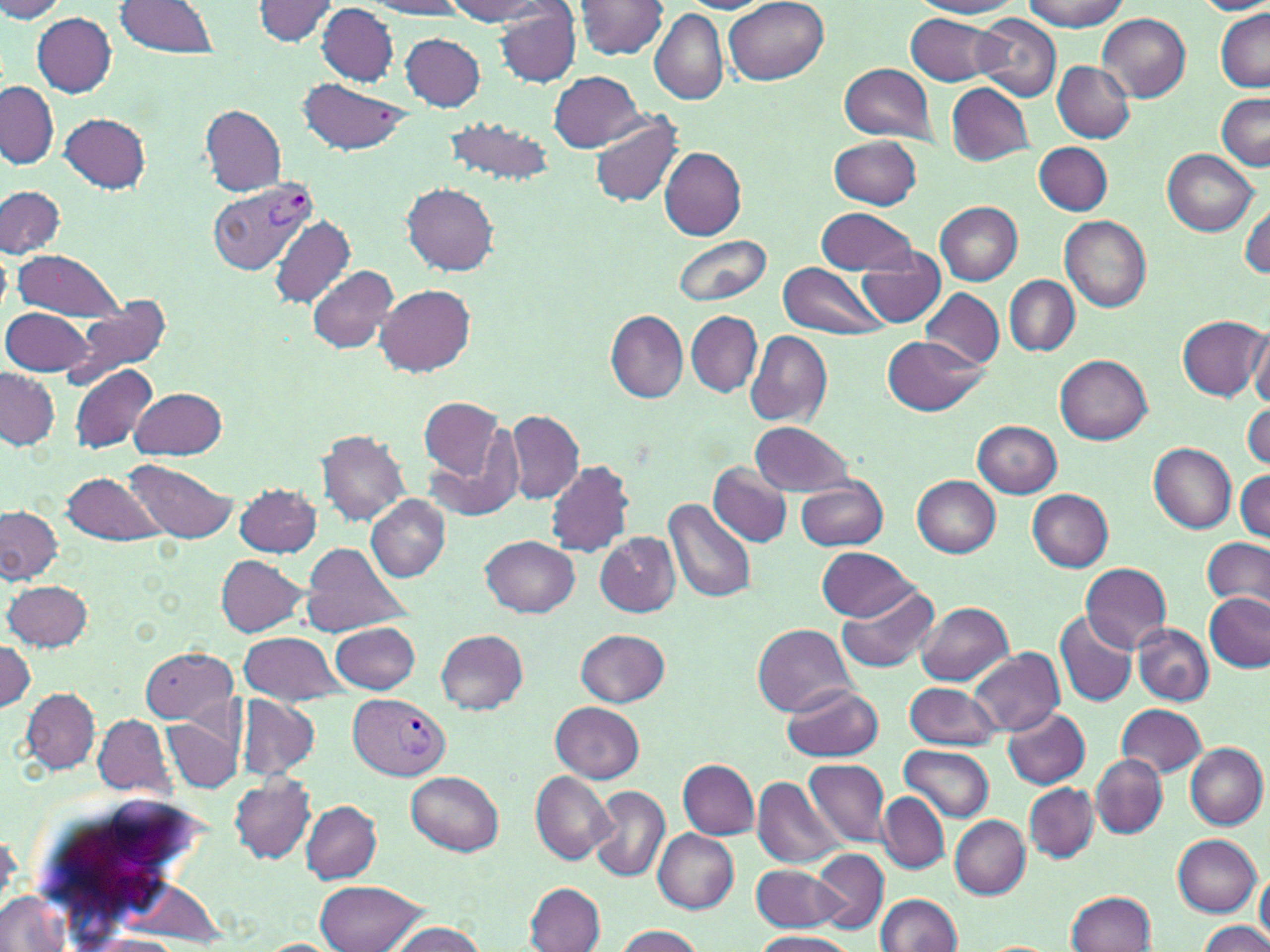

Summary:
  - Coordinate format: approximate bounding boxes as named x1/y1/x2/y2 corners in pixels
  - Plasmodium vivax-infected red blood cell locations: (x1=207, y1=176, x2=321, y2=274), (x1=348, y1=693, x2=449, y2=780)
  - Uninfected red blood cell locations: (x1=0, y1=0, x2=66, y2=23), (x1=251, y1=0, x2=343, y2=46), (x1=368, y1=0, x2=467, y2=18), (x1=446, y1=0, x2=554, y2=23), (x1=724, y1=0, x2=827, y2=85), (x1=914, y1=0, x2=1020, y2=18), (x1=1022, y1=0, x2=1127, y2=31), (x1=116, y1=1, x2=220, y2=56), (x1=576, y1=1, x2=668, y2=59), (x1=1192, y1=1, x2=1270, y2=16), (x1=316, y1=5, x2=399, y2=84), (x1=494, y1=6, x2=580, y2=86), (x1=650, y1=8, x2=729, y2=104), (x1=1216, y1=11, x2=1270, y2=91), (x1=1096, y1=12, x2=1192, y2=101), (x1=32, y1=13, x2=116, y2=97), (x1=906, y1=13, x2=1004, y2=86), (x1=973, y1=15, x2=1062, y2=101), (x1=399, y1=33, x2=486, y2=111), (x1=1051, y1=61, x2=1135, y2=142), (x1=840, y1=63, x2=937, y2=144), (x1=551, y1=71, x2=643, y2=151), (x1=299, y1=78, x2=412, y2=156), (x1=0, y1=81, x2=56, y2=169), (x1=946, y1=82, x2=1034, y2=165), (x1=1217, y1=93, x2=1270, y2=169), (x1=200, y1=105, x2=286, y2=196), (x1=60, y1=113, x2=151, y2=193), (x1=589, y1=113, x2=683, y2=207), (x1=444, y1=118, x2=554, y2=186), (x1=829, y1=136, x2=922, y2=210), (x1=1035, y1=142, x2=1112, y2=215), (x1=659, y1=146, x2=746, y2=240), (x1=1163, y1=149, x2=1259, y2=236), (x1=403, y1=184, x2=498, y2=275), (x1=0, y1=186, x2=66, y2=260), (x1=935, y1=201, x2=1022, y2=285), (x1=1241, y1=205, x2=1270, y2=278), (x1=816, y1=206, x2=919, y2=277), (x1=268, y1=215, x2=354, y2=307), (x1=1060, y1=215, x2=1152, y2=311), (x1=672, y1=232, x2=770, y2=307), (x1=0, y1=246, x2=11, y2=316), (x1=857, y1=249, x2=946, y2=326), (x1=14, y1=250, x2=124, y2=322), (x1=778, y1=261, x2=888, y2=341), (x1=307, y1=264, x2=398, y2=354), (x1=1005, y1=275, x2=1078, y2=354), (x1=375, y1=282, x2=475, y2=376), (x1=920, y1=288, x2=1003, y2=370), (x1=65, y1=294, x2=171, y2=388), (x1=2, y1=307, x2=94, y2=377), (x1=605, y1=310, x2=690, y2=402), (x1=687, y1=312, x2=762, y2=396), (x1=1177, y1=315, x2=1268, y2=400), (x1=1249, y1=329, x2=1270, y2=407), (x1=745, y1=330, x2=832, y2=425), (x1=882, y1=335, x2=988, y2=416), (x1=1056, y1=354, x2=1153, y2=445), (x1=71, y1=363, x2=158, y2=454), (x1=0, y1=367, x2=59, y2=450), (x1=131, y1=386, x2=228, y2=459), (x1=420, y1=399, x2=504, y2=479), (x1=1243, y1=405, x2=1270, y2=468), (x1=505, y1=409, x2=585, y2=502), (x1=973, y1=420, x2=1062, y2=497), (x1=752, y1=421, x2=854, y2=498), (x1=317, y1=431, x2=410, y2=525), (x1=423, y1=438, x2=523, y2=522), (x1=1149, y1=443, x2=1237, y2=532), (x1=546, y1=459, x2=634, y2=558), (x1=123, y1=460, x2=237, y2=544), (x1=708, y1=463, x2=794, y2=547), (x1=1234, y1=468, x2=1270, y2=541), (x1=60, y1=470, x2=164, y2=546), (x1=913, y1=475, x2=1001, y2=557), (x1=795, y1=478, x2=888, y2=551), (x1=234, y1=483, x2=321, y2=557), (x1=1028, y1=488, x2=1114, y2=572), (x1=366, y1=494, x2=450, y2=581), (x1=662, y1=497, x2=757, y2=603), (x1=0, y1=507, x2=61, y2=583), (x1=596, y1=532, x2=680, y2=617), (x1=480, y1=536, x2=581, y2=617), (x1=1204, y1=539, x2=1270, y2=611), (x1=298, y1=542, x2=411, y2=638), (x1=816, y1=547, x2=917, y2=620), (x1=217, y1=554, x2=311, y2=637), (x1=1080, y1=563, x2=1172, y2=653), (x1=4, y1=580, x2=91, y2=652), (x1=835, y1=582, x2=940, y2=673), (x1=1204, y1=593, x2=1269, y2=671), (x1=916, y1=602, x2=1012, y2=685), (x1=1054, y1=609, x2=1137, y2=709), (x1=329, y1=621, x2=420, y2=694), (x1=1132, y1=622, x2=1213, y2=705), (x1=752, y1=623, x2=858, y2=716), (x1=576, y1=629, x2=669, y2=706), (x1=435, y1=630, x2=528, y2=714), (x1=237, y1=631, x2=346, y2=704), (x1=1, y1=638, x2=35, y2=712), (x1=140, y1=645, x2=237, y2=724), (x1=969, y1=647, x2=1065, y2=737), (x1=904, y1=681, x2=1002, y2=751), (x1=783, y1=683, x2=886, y2=762), (x1=21, y1=688, x2=100, y2=774), (x1=236, y1=695, x2=319, y2=782), (x1=551, y1=701, x2=645, y2=782), (x1=1116, y1=703, x2=1208, y2=777), (x1=1003, y1=708, x2=1090, y2=788), (x1=91, y1=714, x2=177, y2=800), (x1=162, y1=716, x2=242, y2=792), (x1=900, y1=744, x2=995, y2=821), (x1=1186, y1=744, x2=1268, y2=829), (x1=1091, y1=756, x2=1167, y2=838), (x1=678, y1=758, x2=758, y2=839), (x1=807, y1=758, x2=890, y2=846), (x1=407, y1=771, x2=503, y2=855), (x1=529, y1=772, x2=616, y2=864), (x1=230, y1=775, x2=315, y2=864), (x1=753, y1=778, x2=846, y2=868), (x1=1025, y1=783, x2=1097, y2=863), (x1=589, y1=784, x2=670, y2=883), (x1=877, y1=791, x2=950, y2=875), (x1=301, y1=800, x2=382, y2=883), (x1=950, y1=816, x2=1030, y2=897), (x1=654, y1=828, x2=738, y2=913), (x1=1173, y1=835, x2=1261, y2=916), (x1=813, y1=850, x2=888, y2=931), (x1=752, y1=862, x2=848, y2=933), (x1=1256, y1=869, x2=1269, y2=946), (x1=315, y1=881, x2=429, y2=951), (x1=526, y1=883, x2=605, y2=951), (x1=1065, y1=891, x2=1157, y2=952), (x1=0, y1=892, x2=71, y2=951), (x1=875, y1=893, x2=962, y2=951), (x1=387, y1=922, x2=486, y2=952), (x1=1200, y1=922, x2=1270, y2=952), (x1=612, y1=925, x2=705, y2=952), (x1=751, y1=931, x2=856, y2=952), (x1=83, y1=935, x2=187, y2=951)
  - White blood cell locations: (x1=19, y1=788, x2=229, y2=942)
  - Slide-level diagnosis: Plasmodium vivax
  - Modality: light microscopy
  - Magnification: 1000x
  - Field of view: single
  - Preparation: thin blood film
  - Image size: 1270×952 pixels
  - Stain: May-Grünwald-Giemsa